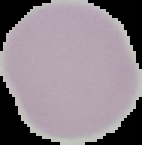
Summary:
  - Malaria status: uninfected
  - Image type: segmented cell region with the area outside set to black
  - Preparation: thin blood smear
  - Image size: 142×145 pixels